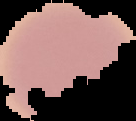
{
  "result": "Plasmodium parasites identified",
  "image_type": "segmented cell region with the area outside set to black",
  "preparation": "thin blood film",
  "image_size": "136×121 pixels"
}